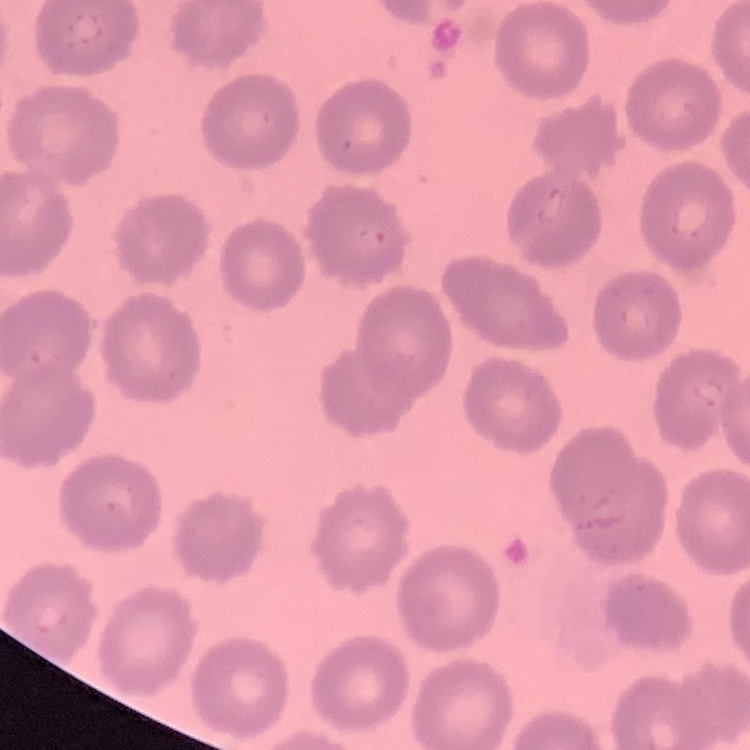
red_blood_cell_morphology: no rouleaux formation
preparation: thin blood smear
image_type: square crop of a larger photomicrograph
stain: Field's or Giemsa